Name the blood parasite species.
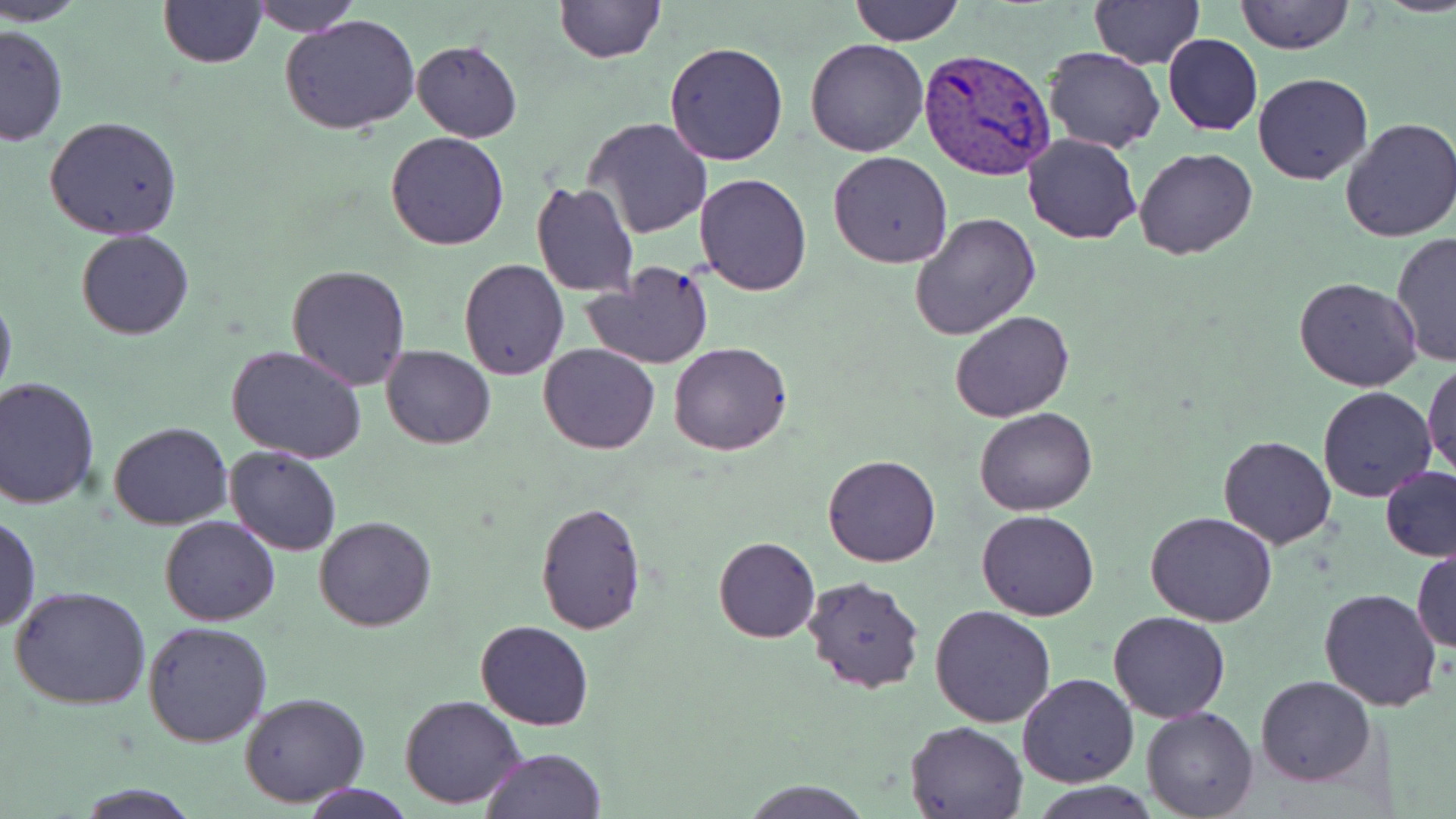

Plasmodium vivax.

Approximate bounding boxes as named x1/y1/x2/y2 corners in pixels. Uninfected red blood cell locations: (x1=4, y1=0, x2=89, y2=26), (x1=158, y1=0, x2=268, y2=68), (x1=251, y1=0, x2=360, y2=36), (x1=554, y1=0, x2=665, y2=64), (x1=851, y1=0, x2=964, y2=45), (x1=1090, y1=0, x2=1202, y2=68), (x1=1235, y1=0, x2=1353, y2=54), (x1=280, y1=15, x2=423, y2=134), (x1=0, y1=23, x2=70, y2=147), (x1=1164, y1=34, x2=1262, y2=136), (x1=805, y1=36, x2=929, y2=156), (x1=411, y1=39, x2=522, y2=142), (x1=664, y1=41, x2=790, y2=167), (x1=1043, y1=46, x2=1164, y2=152), (x1=1252, y1=73, x2=1374, y2=186), (x1=42, y1=116, x2=184, y2=241), (x1=581, y1=117, x2=714, y2=240), (x1=1337, y1=117, x2=1456, y2=243), (x1=385, y1=132, x2=509, y2=251), (x1=1022, y1=132, x2=1141, y2=244), (x1=1134, y1=146, x2=1256, y2=260), (x1=828, y1=150, x2=953, y2=269), (x1=693, y1=173, x2=813, y2=296), (x1=529, y1=180, x2=639, y2=298), (x1=909, y1=211, x2=1041, y2=341), (x1=77, y1=229, x2=193, y2=339), (x1=1390, y1=230, x2=1456, y2=367), (x1=458, y1=259, x2=569, y2=381), (x1=580, y1=262, x2=715, y2=369), (x1=287, y1=264, x2=413, y2=390), (x1=1294, y1=276, x2=1422, y2=390), (x1=0, y1=289, x2=16, y2=412), (x1=950, y1=310, x2=1074, y2=421), (x1=539, y1=342, x2=659, y2=454), (x1=668, y1=342, x2=793, y2=457), (x1=226, y1=345, x2=369, y2=464), (x1=382, y1=345, x2=495, y2=449), (x1=1422, y1=360, x2=1455, y2=479), (x1=0, y1=378, x2=101, y2=509), (x1=1317, y1=384, x2=1437, y2=503), (x1=974, y1=406, x2=1097, y2=516), (x1=109, y1=421, x2=232, y2=530), (x1=1218, y1=435, x2=1339, y2=549), (x1=224, y1=443, x2=342, y2=555), (x1=823, y1=454, x2=940, y2=567), (x1=1378, y1=464, x2=1456, y2=562), (x1=535, y1=502, x2=646, y2=633), (x1=977, y1=510, x2=1100, y2=620), (x1=1, y1=511, x2=41, y2=634), (x1=1146, y1=511, x2=1277, y2=626), (x1=159, y1=514, x2=281, y2=627), (x1=314, y1=515, x2=436, y2=631), (x1=713, y1=535, x2=820, y2=642), (x1=1412, y1=544, x2=1455, y2=656), (x1=800, y1=574, x2=925, y2=694), (x1=10, y1=586, x2=152, y2=712), (x1=1318, y1=587, x2=1443, y2=712), (x1=930, y1=606, x2=1057, y2=728), (x1=1109, y1=612, x2=1229, y2=723), (x1=474, y1=619, x2=595, y2=730), (x1=143, y1=621, x2=274, y2=747), (x1=1017, y1=673, x2=1139, y2=788), (x1=1255, y1=675, x2=1377, y2=787), (x1=240, y1=691, x2=369, y2=807), (x1=399, y1=694, x2=527, y2=808), (x1=1141, y1=706, x2=1258, y2=818), (x1=905, y1=720, x2=1030, y2=818), (x1=482, y1=748, x2=604, y2=819), (x1=301, y1=781, x2=414, y2=819), (x1=744, y1=781, x2=868, y2=817), (x1=77, y1=783, x2=201, y2=818), (x1=1034, y1=783, x2=1159, y2=818). Plasmodium vivax-infected red blood cell locations: (x1=918, y1=46, x2=1057, y2=180). May-Grünwald-Giemsa stain. 1000x magnification. Thin blood film. Light microscopy. Image is 1456×819 pixels. Single field of view.